State the blood parasite species.
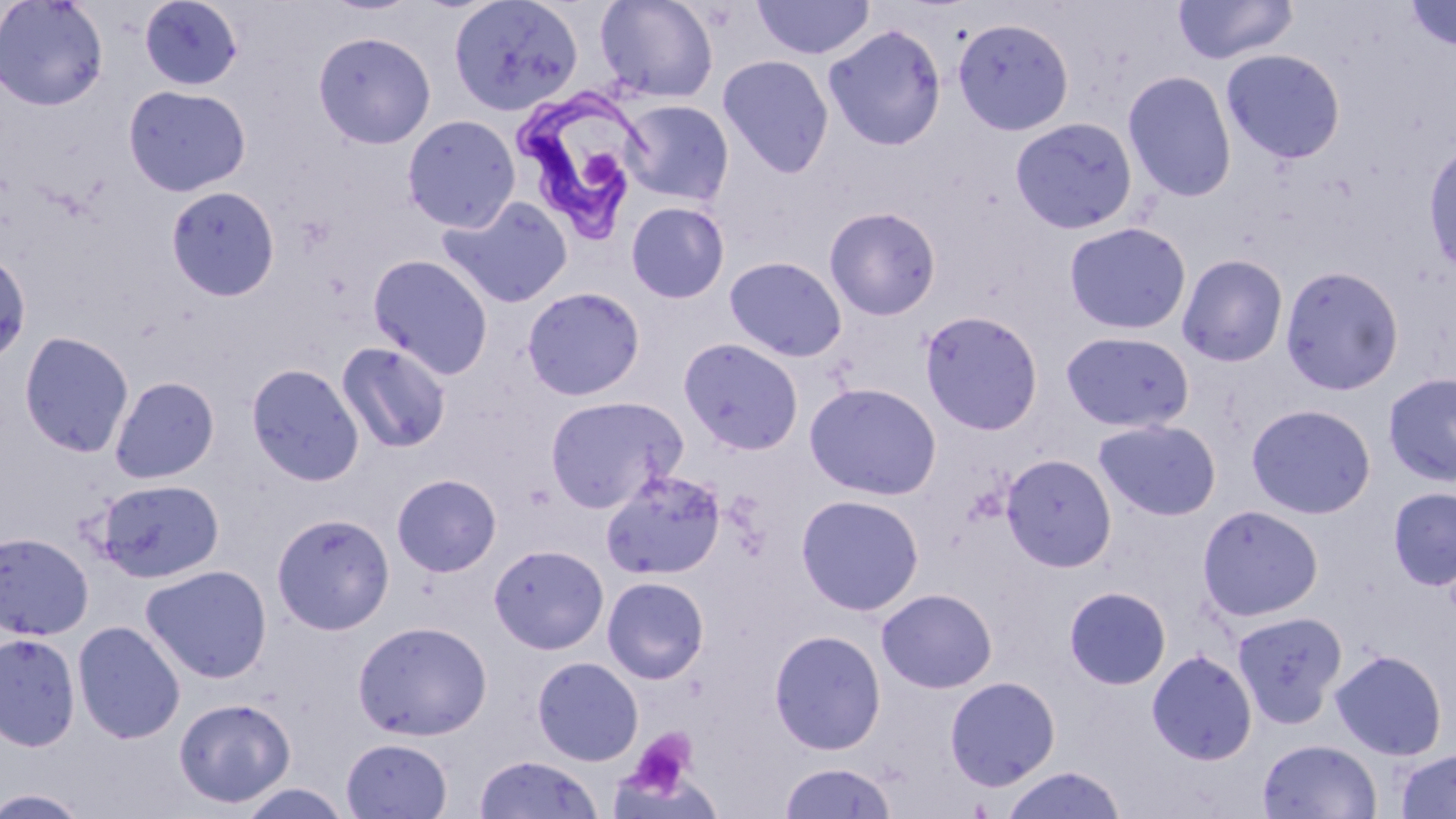

Trypanosoma brucei.

Approximate bounding boxes as (x1, y1, x2, y2) in pixels. Trypanosoma brucei locations: (509, 85, 648, 243). Platelet locations: (587, 151, 618, 186), (623, 728, 700, 801). Uninfected red blood cell locations: (0, 0, 109, 111), (139, 0, 244, 90), (448, 0, 584, 117), (595, 0, 719, 104), (751, 0, 875, 60), (1172, 0, 1299, 65), (1402, 1, 1456, 52), (953, 17, 1074, 136), (823, 24, 946, 151), (313, 30, 436, 149), (1221, 48, 1347, 164), (717, 55, 835, 178), (1122, 70, 1237, 203), (123, 84, 251, 197), (620, 99, 734, 206), (401, 115, 521, 232), (1009, 116, 1138, 235), (1423, 138, 1456, 282), (165, 185, 280, 301), (437, 195, 574, 309), (625, 200, 730, 304), (824, 206, 942, 321), (1064, 221, 1192, 335), (0, 250, 31, 365), (1177, 253, 1289, 367), (368, 254, 493, 379), (723, 255, 848, 362), (1279, 265, 1404, 396), (522, 286, 646, 400), (919, 310, 1044, 436), (1059, 330, 1195, 433), (19, 331, 135, 458), (678, 337, 804, 456), (336, 340, 452, 454), (246, 363, 364, 486), (1382, 372, 1456, 486), (109, 376, 220, 485), (804, 382, 942, 501), (544, 395, 686, 512), (1246, 403, 1377, 519), (1094, 419, 1221, 521), (1000, 453, 1117, 572), (600, 469, 727, 581), (391, 473, 502, 577), (94, 478, 225, 583), (1388, 487, 1456, 590), (795, 494, 924, 615), (1196, 504, 1324, 622), (271, 513, 395, 635), (0, 532, 94, 640), (488, 544, 609, 654), (140, 564, 272, 683), (602, 576, 709, 684), (1064, 585, 1171, 690), (876, 588, 997, 693), (1232, 611, 1348, 727), (353, 620, 492, 740), (73, 621, 186, 744), (768, 629, 886, 755), (0, 632, 81, 752), (1146, 649, 1257, 765), (1330, 649, 1447, 760), (532, 656, 644, 766), (944, 675, 1061, 791), (173, 697, 295, 808), (341, 737, 453, 818), (1257, 738, 1383, 819), (1394, 748, 1456, 818), (474, 754, 602, 818), (777, 761, 898, 819), (999, 766, 1128, 819), (0, 787, 92, 818). Image is 1456×819 pixels. Light microscopy. Thin blood film. May-Grünwald-Giemsa-stained preparation. Captured at 1000x magnification. One field of a larger specimen.